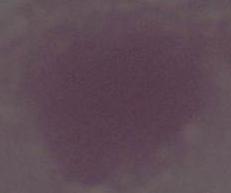
1000x magnification. Photomicrograph. A red blood cell is shown.